Classify this cell by malaria status.
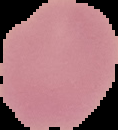
Uninfected.

From a thin blood smear. Segmented cell region on a black background. Image is 118×130 pixels.